Give the extent of all uninfected red blood cells.
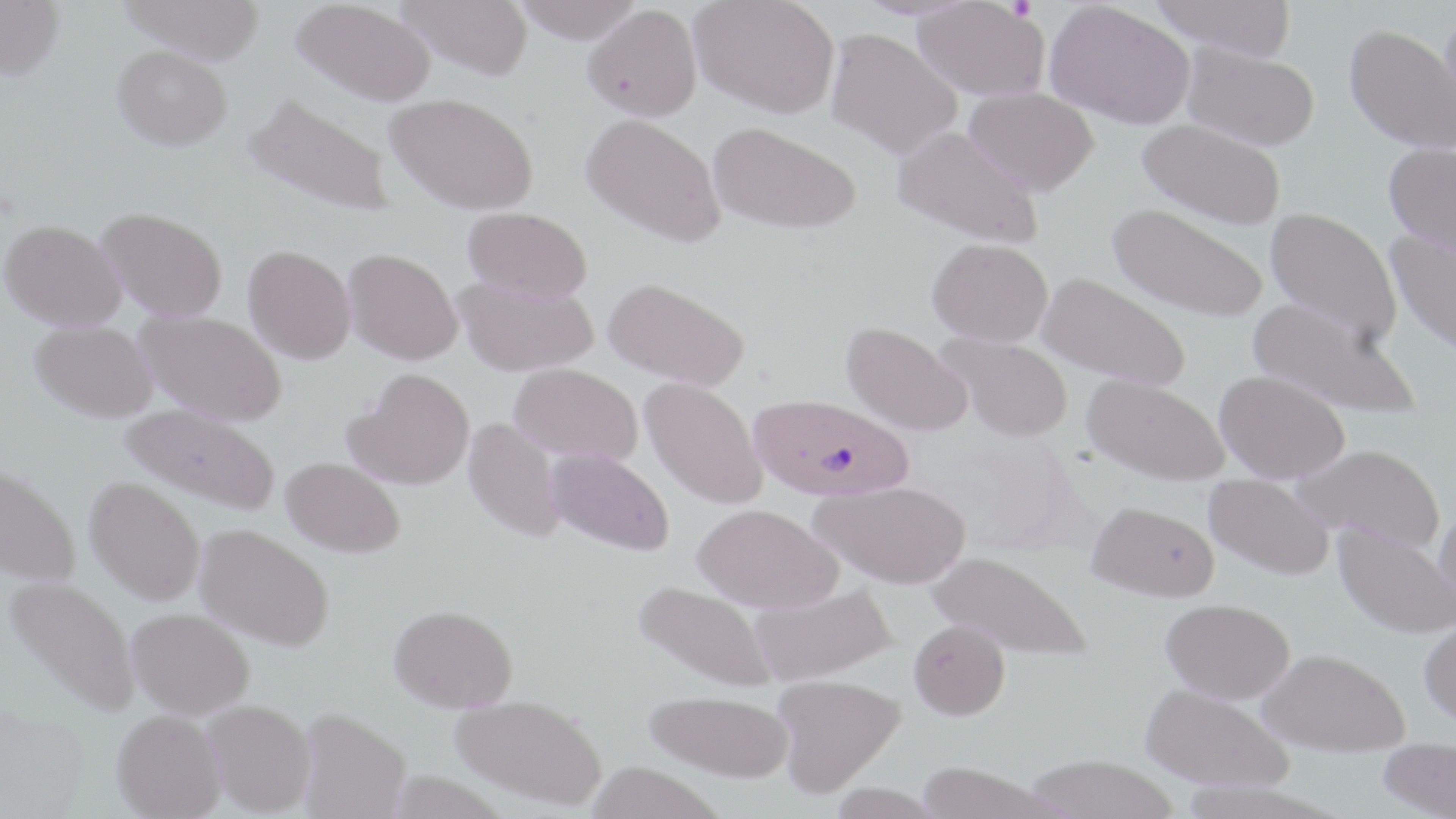

Approximate bounding boxes as (x1,y1)-(x2,y2) corner pairs in pixels.
Uninfected red blood cells: (118,0)-(267,63), (398,0)-(534,80), (511,0)-(644,43), (690,0)-(839,118), (913,0)-(1048,100), (1151,0)-(1297,61), (0,1)-(64,82), (293,1)-(435,106), (1045,2)-(1195,131), (582,4)-(701,122), (1343,27)-(1456,156), (826,28)-(961,159), (112,45)-(232,150), (1182,45)-(1318,153), (964,87)-(1099,197), (386,92)-(539,215), (243,93)-(396,218), (581,113)-(725,246), (1137,120)-(1285,232), (708,122)-(861,235), (892,125)-(1042,248), (1383,144)-(1456,260), (1108,206)-(1268,324), (97,207)-(228,321), (462,207)-(592,304), (1264,209)-(1401,347), (0,219)-(126,330), (1385,230)-(1456,359), (927,240)-(1053,348), (242,245)-(356,364), (343,248)-(463,365), (454,274)-(598,376), (1036,274)-(1191,390), (603,278)-(750,390), (1246,298)-(1420,422), (135,310)-(287,426), (30,320)-(158,422), (839,322)-(973,437), (936,332)-(1073,443), (509,363)-(643,463), (345,367)-(475,490), (1214,371)-(1349,484), (1083,375)-(1229,486), (640,378)-(767,509), (121,403)-(281,515), (463,417)-(565,543), (1292,445)-(1444,554), (545,447)-(675,556), (281,457)-(405,558), (0,463)-(81,587), (1204,474)-(1335,580), (84,476)-(206,605), (811,481)-(970,588), (1087,501)-(1219,602), (1433,503)-(1456,623), (693,504)-(844,613), (1333,522)-(1456,640), (195,524)-(334,651), (927,549)-(1091,661), (4,576)-(140,717), (633,580)-(778,692), (749,583)-(898,685), (1161,598)-(1295,704), (389,604)-(518,712), (128,608)-(254,718), (1419,617)-(1456,729), (908,619)-(1010,720), (1259,648)-(1409,755), (772,674)-(906,797), (1140,684)-(1292,792), (644,690)-(794,782), (451,694)-(607,810), (203,700)-(316,816), (297,707)-(411,819), (111,710)-(226,818), (1378,739)-(1456,818), (1024,755)-(1178,819), (585,762)-(729,819), (915,762)-(1054,819).

Plasmodium falciparum-infected red blood cell locations: (748,394)-(913,501). Slide-level diagnosis: Plasmodium falciparum. Single field of view. Captured at 1000x magnification. May-Grünwald-Giemsa stain. Thin blood smear. Image is 1456×819 pixels. Optical microscopy.